Evaluate for Plasmodium parasites.
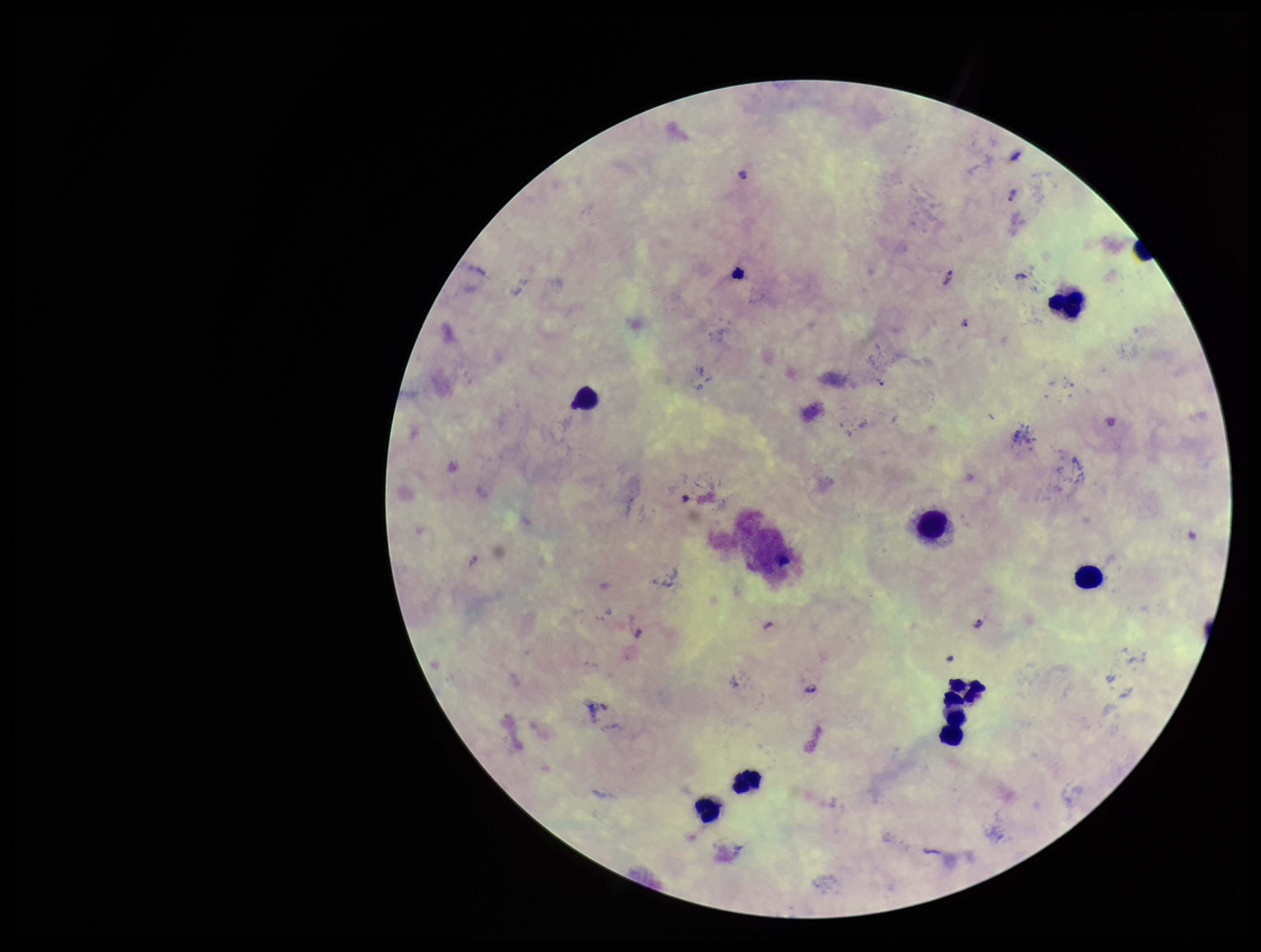
Identified.

image size = 1261×952 pixels
parasite count = 6
capture = smartphone photograph through the microscope eyepiece
preparation = thick smear
species reported for this patient = Plasmodium falciparum
patient malaria status = positive
stain = Giemsa
leukocyte count = 8
field of view = single